State the blood parasite species.
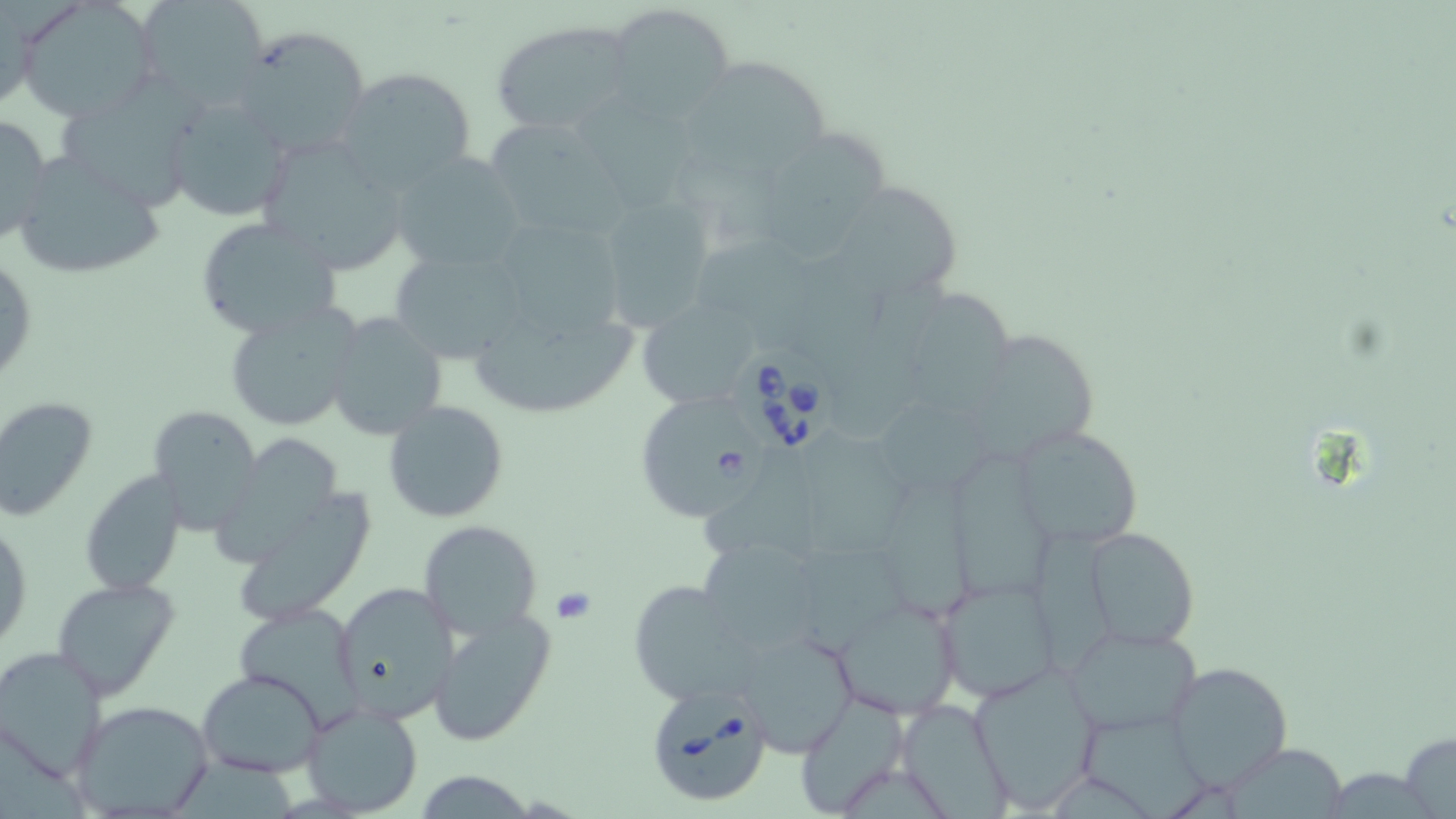

Babesia divergens.

Summary:
  - Coordinate format: approximate bounding boxes as (x1,y1)-(x2,y2) corner pairs in pixels
  - Babesia divergens-infected red blood cell locations: (737,346)-(838,457), (632,394)-(769,522), (644,684)-(774,809)
  - Uninfected red blood cell locations: (137,0)-(269,107), (16,1)-(158,122), (607,3)-(733,121), (490,21)-(636,134), (233,26)-(372,158), (698,60)-(833,163), (334,65)-(478,195), (570,90)-(693,211), (165,95)-(292,222), (59,99)-(189,216), (0,112)-(52,248), (483,116)-(624,237), (764,132)-(895,263), (255,133)-(411,276), (7,150)-(169,281), (391,151)-(527,275), (824,174)-(963,299), (587,194)-(720,331), (193,217)-(343,338), (504,224)-(626,331), (691,237)-(833,329), (390,245)-(531,366), (1,249)-(37,390), (901,289)-(1022,414), (636,298)-(765,411), (463,299)-(640,420), (223,302)-(362,432), (325,310)-(447,440), (958,330)-(1095,464), (0,396)-(98,522), (383,399)-(510,522), (145,403)-(263,534), (1013,424)-(1143,551), (800,430)-(917,558), (208,434)-(352,570), (704,458)-(831,564), (952,464)-(1053,600), (79,470)-(187,597), (886,482)-(975,619), (225,485)-(377,631), (1,515)-(32,658), (417,519)-(544,639), (1033,528)-(1116,677), (1083,528)-(1201,651), (694,537)-(828,656), (802,542)-(912,657), (53,576)-(179,699), (936,576)-(1060,703), (331,578)-(459,726), (626,579)-(764,707), (831,595)-(963,718), (233,602)-(368,727), (427,607)-(556,747), (1064,622)-(1202,736), (734,625)-(858,756), (0,646)-(106,780), (1163,660)-(1293,791), (968,665)-(1102,812), (197,668)-(328,778), (795,695)-(908,817), (895,697)-(1012,819), (68,698)-(217,819), (300,700)-(423,816), (1084,712)-(1211,818), (0,725)-(87,819), (1397,729)-(1456,819), (1228,742)-(1347,816), (174,757)-(296,819), (1325,772)-(1445,819)
  - Preparation: thin blood film
  - Field of view: one of a larger specimen
  - Modality: optical microscopy
  - Magnification: 1000x
  - Image size: 1456×819 pixels
  - Stain: May-Grünwald-Giemsa